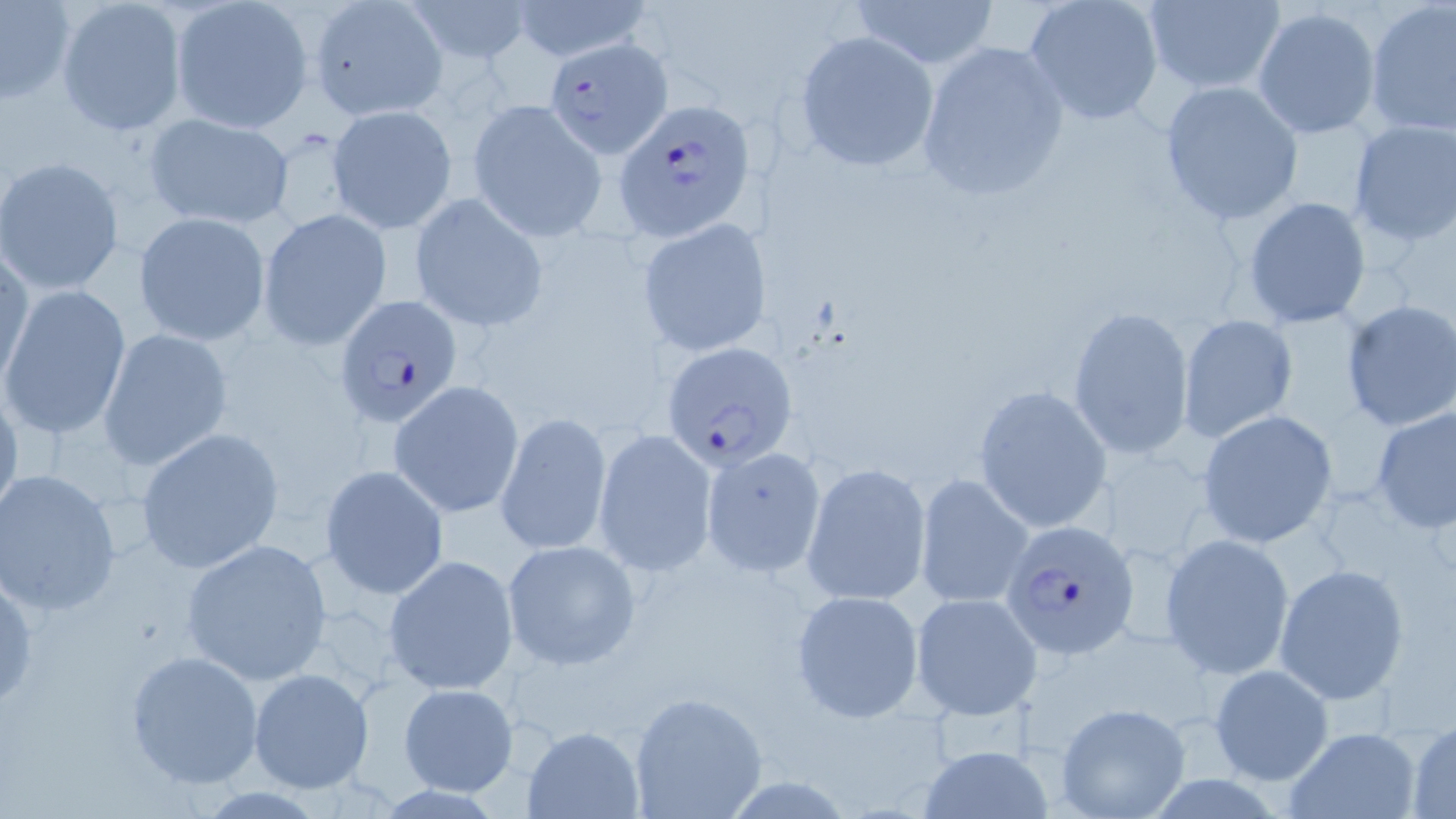

Summary:
  - Coordinate format: approximate bounding boxes as [x1, y1, x2, y2] in pixels
  - Uninfected red blood cell locations: [56, 0, 187, 136], [169, 0, 312, 134], [404, 0, 533, 59], [507, 0, 649, 61], [848, 0, 1000, 70], [1023, 0, 1166, 126], [1140, 0, 1286, 92], [1, 1, 76, 104], [309, 1, 446, 122], [1364, 1, 1455, 139], [1251, 6, 1382, 139], [794, 30, 940, 173], [914, 39, 1070, 202], [1157, 80, 1305, 226], [467, 99, 606, 242], [327, 105, 457, 233], [142, 110, 296, 232], [1346, 119, 1456, 247], [1, 158, 125, 295], [1240, 195, 1372, 330], [411, 196, 548, 329], [259, 209, 392, 349], [135, 213, 270, 346], [638, 219, 769, 357], [1, 241, 32, 391], [0, 285, 132, 442], [1340, 301, 1456, 431], [1067, 304, 1194, 457], [1177, 314, 1300, 443], [98, 328, 233, 474], [0, 378, 22, 532], [389, 381, 524, 517], [973, 384, 1110, 533], [1369, 403, 1455, 534], [1195, 409, 1340, 550], [493, 412, 614, 556], [135, 428, 284, 574], [593, 429, 717, 577], [699, 444, 827, 579], [800, 460, 931, 607], [320, 464, 447, 599], [0, 469, 124, 618], [914, 472, 1034, 610], [1159, 535, 1296, 680], [180, 538, 334, 684], [501, 539, 641, 669], [383, 554, 520, 696], [1272, 562, 1409, 706], [1, 566, 40, 715], [790, 590, 925, 721], [911, 592, 1042, 719], [124, 649, 264, 788], [1208, 664, 1335, 786], [249, 668, 375, 795], [397, 683, 518, 798], [627, 691, 768, 819], [1054, 701, 1191, 819], [1406, 718, 1456, 819], [522, 726, 647, 819], [1283, 727, 1423, 819], [916, 743, 1055, 819]
  - Plasmodium falciparum-infected red blood cell locations: [545, 36, 674, 159], [613, 98, 756, 239], [332, 294, 465, 428], [661, 343, 798, 467], [1000, 520, 1141, 659]
  - Slide-level diagnosis: Plasmodium falciparum
  - Image size: 1456×819 pixels
  - Stain: May-Grünwald-Giemsa
  - Preparation: thin blood smear
  - Modality: optical microscopy
  - Magnification: 1000x
  - Field of view: one of a larger specimen